Outline each blood parasite and name the species.
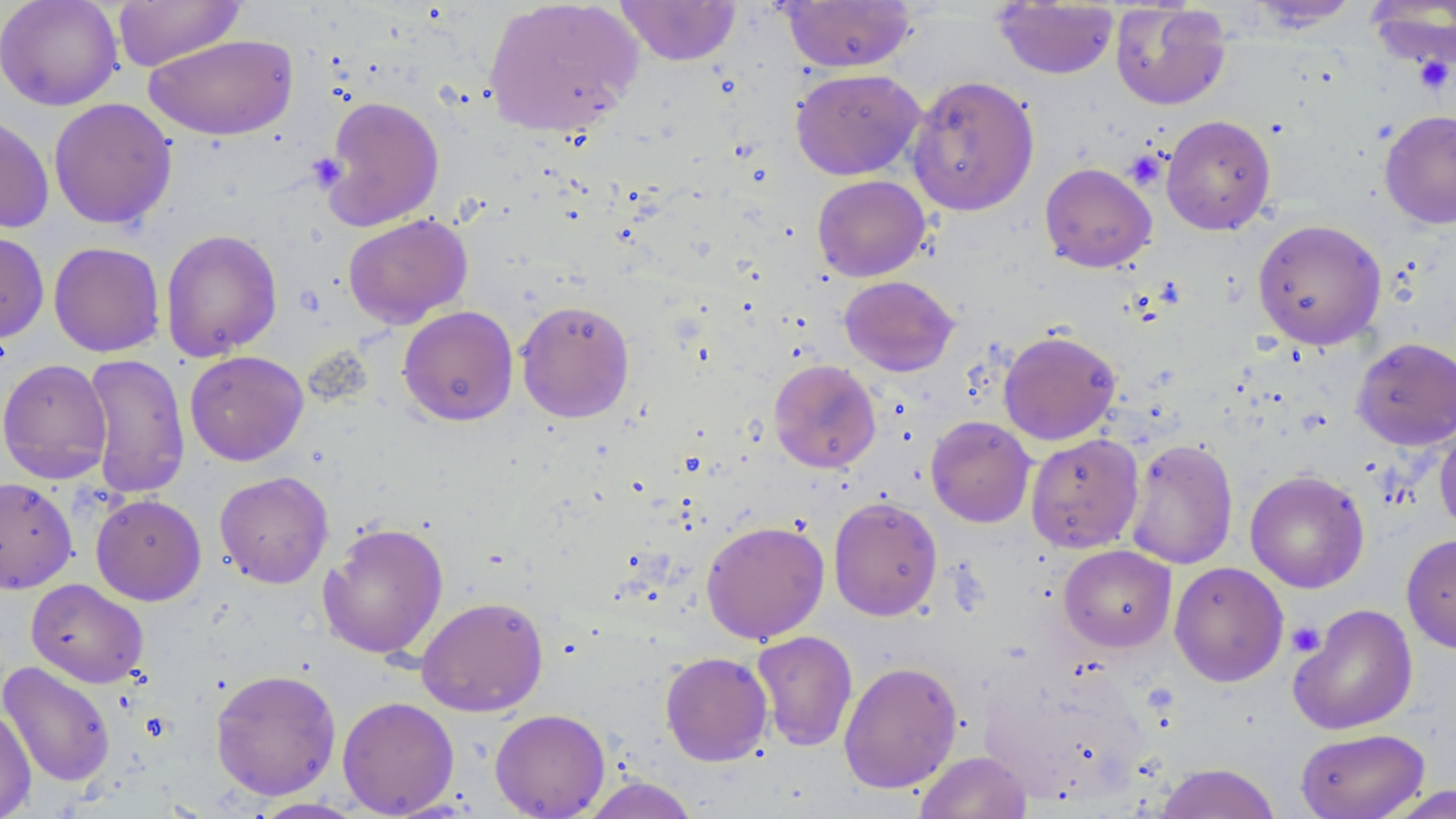
No blood parasites observed.

Summary:
  - Coordinate format: approximate bounding boxes as (x1,y1)-(x2,y2) corner pairs in pixels
  - Uninfected red blood cell locations: (0,0)-(123,111), (112,0)-(246,71), (483,0)-(644,139), (779,0)-(918,73), (1246,0)-(1364,29), (613,1)-(742,65), (992,1)-(1119,80), (1365,1)-(1456,73), (1110,2)-(1232,111), (144,33)-(299,141), (790,68)-(925,180), (906,74)-(1040,217), (319,95)-(445,231), (47,97)-(178,229), (1379,109)-(1456,229), (0,112)-(54,234), (1160,115)-(1276,235), (1039,162)-(1156,272), (812,175)-(930,281), (343,213)-(472,328), (1252,219)-(1387,350), (0,228)-(50,344), (160,228)-(282,361), (48,241)-(165,357), (839,275)-(959,376), (515,299)-(635,423), (397,305)-(519,426), (998,329)-(1121,445), (1352,337)-(1456,450), (184,350)-(309,466), (83,353)-(190,500), (0,358)-(113,484), (768,358)-(882,473), (926,416)-(1036,527), (1434,423)-(1456,540), (1026,433)-(1144,553), (1124,438)-(1238,570), (1245,469)-(1369,593), (214,471)-(334,589), (0,477)-(77,594), (90,494)-(206,605), (828,497)-(942,621), (701,519)-(829,645), (317,521)-(449,660), (1402,533)-(1456,654), (1058,545)-(1176,651), (1169,561)-(1289,686), (25,578)-(149,688), (416,595)-(549,717), (1288,603)-(1418,736), (752,630)-(858,752), (660,651)-(773,766), (978,657)-(1147,804), (1,660)-(116,788), (838,660)-(963,793), (210,667)-(341,800), (337,696)-(459,817), (0,707)-(36,819), (490,708)-(610,818), (1295,727)-(1430,819), (913,751)-(1032,819), (1153,762)-(1282,819), (579,775)-(701,819), (1380,785)-(1456,818), (248,797)-(368,819)
  - Platelet locations: (1412,56)-(1454,95), (1124,149)-(1167,190), (1286,621)-(1326,657)
  - Slide-level diagnosis: negative for blood parasites
  - Preparation: thin blood film
  - Field of view: one of a larger specimen
  - Modality: light microscopy
  - Image size: 1456×819 pixels
  - Stain: May-Grünwald-Giemsa
  - Magnification: 1000x